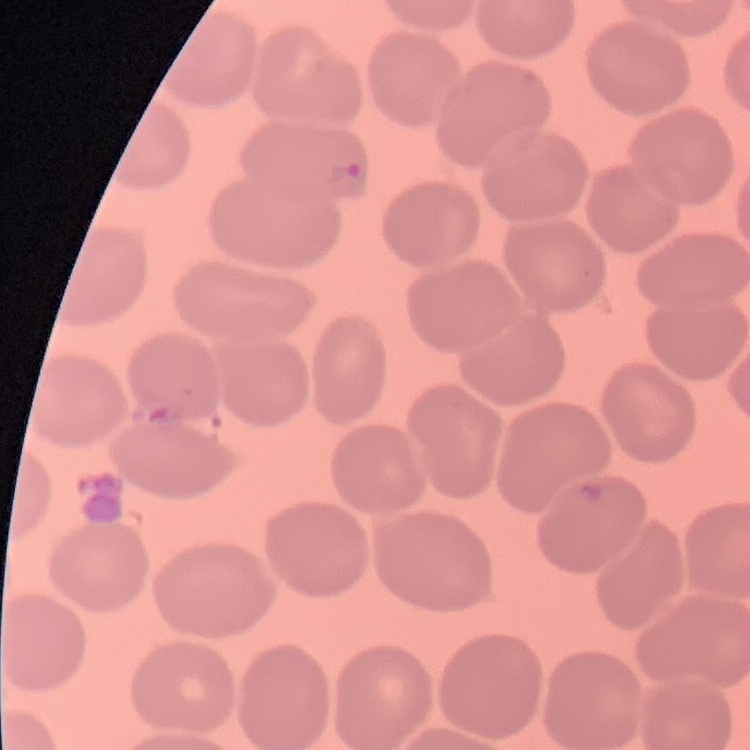
red_blood_cell_morphology: no rouleaux formation
preparation: thin blood film
stain: Field's or Giemsa
image_type: square crop of a larger photomicrograph